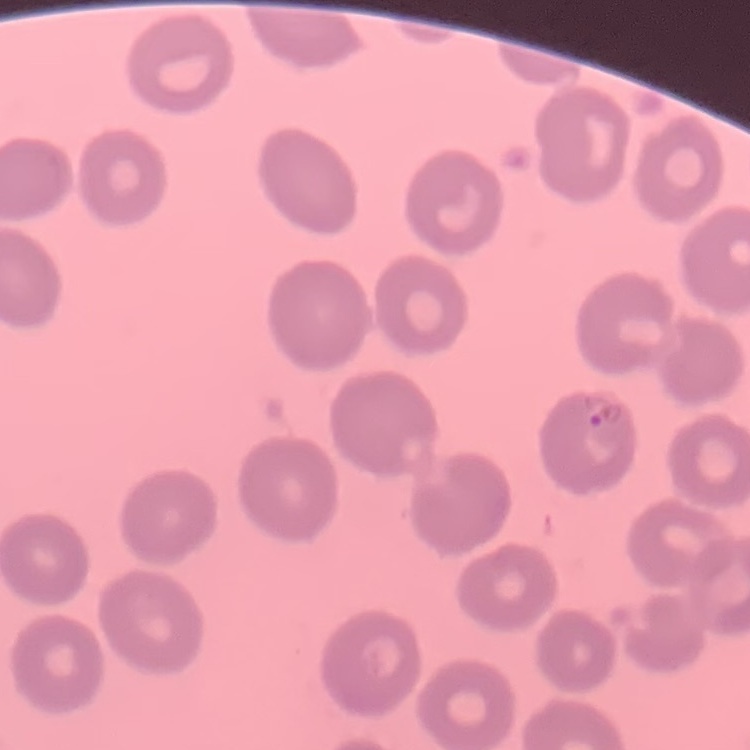

Summary:
  - Erythrocyte morphology: no rouleaux formation
  - Stain: Field's or Giemsa
  - Image type: square crop of a larger photomicrograph
  - Preparation: thin blood smear